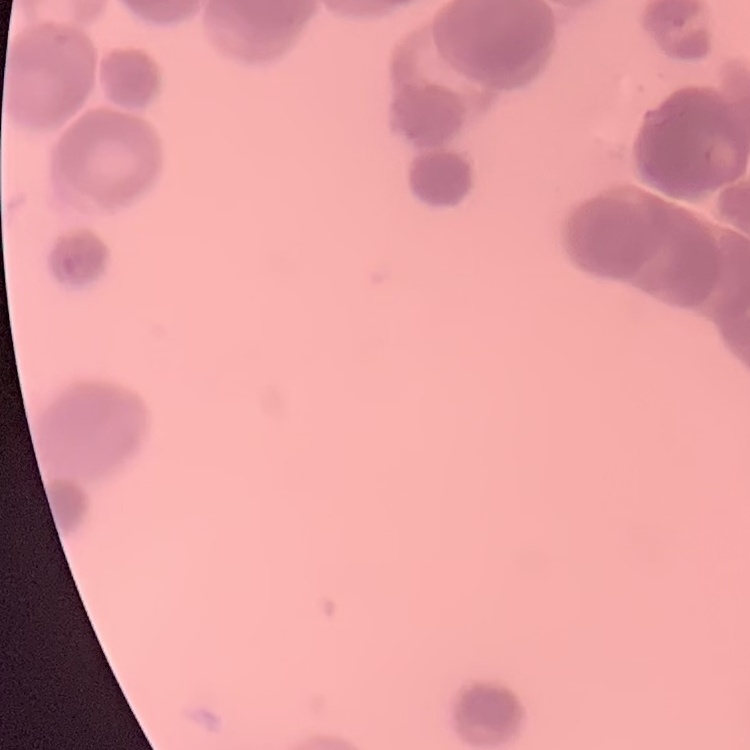
{
  "erythrocyte_morphology": "rouleaux formation",
  "preparation": "thin blood smear",
  "stain": "Field's or Giemsa",
  "image_type": "one tile cut from a larger photomicrograph"
}